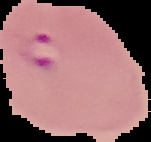
The area outside the segmented cell region is set to black. Malaria status: parasitized. From a thin blood smear. Image is 151×142 pixels.